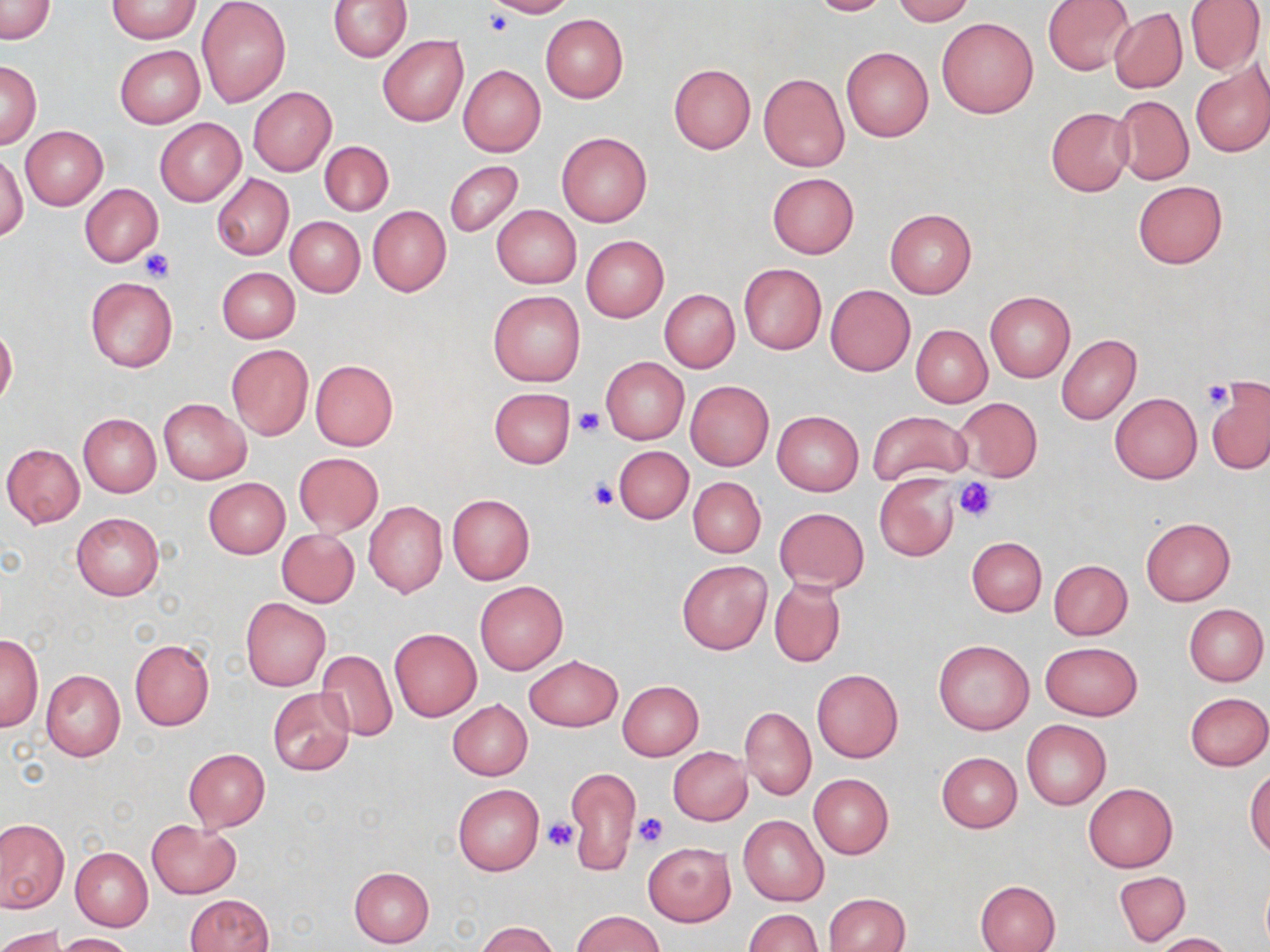

slide-level diagnosis = negative for blood parasites
uninfected red blood cell locations = approximate bounding boxes as named x1/y1/x2/y2 corners in pixels: (x1=108, y1=0, x2=200, y2=43), (x1=196, y1=0, x2=290, y2=107), (x1=483, y1=0, x2=576, y2=18), (x1=804, y1=0, x2=894, y2=16), (x1=890, y1=0, x2=974, y2=24), (x1=1043, y1=0, x2=1135, y2=74), (x1=1185, y1=0, x2=1265, y2=76), (x1=0, y1=1, x2=55, y2=43), (x1=329, y1=1, x2=412, y2=61), (x1=1109, y1=8, x2=1187, y2=93), (x1=540, y1=14, x2=628, y2=103), (x1=937, y1=17, x2=1039, y2=118), (x1=377, y1=36, x2=469, y2=126), (x1=115, y1=45, x2=205, y2=128), (x1=841, y1=47, x2=933, y2=141), (x1=1, y1=61, x2=41, y2=148), (x1=668, y1=63, x2=756, y2=153), (x1=1191, y1=64, x2=1270, y2=157), (x1=458, y1=65, x2=546, y2=158), (x1=759, y1=73, x2=849, y2=171), (x1=248, y1=86, x2=335, y2=176), (x1=1113, y1=95, x2=1194, y2=186), (x1=1045, y1=107, x2=1134, y2=196), (x1=155, y1=118, x2=245, y2=206), (x1=21, y1=126, x2=108, y2=210), (x1=557, y1=132, x2=652, y2=227), (x1=319, y1=141, x2=392, y2=216), (x1=0, y1=151, x2=26, y2=242), (x1=444, y1=160, x2=523, y2=237), (x1=210, y1=173, x2=294, y2=261), (x1=766, y1=173, x2=858, y2=259), (x1=1132, y1=180, x2=1227, y2=269), (x1=80, y1=183, x2=162, y2=267), (x1=491, y1=205, x2=581, y2=289), (x1=368, y1=206, x2=451, y2=296), (x1=885, y1=209, x2=977, y2=298), (x1=285, y1=216, x2=365, y2=297), (x1=581, y1=236, x2=669, y2=323), (x1=739, y1=263, x2=826, y2=354), (x1=217, y1=267, x2=299, y2=343), (x1=84, y1=276, x2=178, y2=373), (x1=825, y1=284, x2=916, y2=376), (x1=488, y1=290, x2=585, y2=386), (x1=660, y1=290, x2=739, y2=372), (x1=985, y1=291, x2=1075, y2=382), (x1=0, y1=324, x2=17, y2=407), (x1=911, y1=325, x2=992, y2=407), (x1=1057, y1=335, x2=1142, y2=425), (x1=226, y1=343, x2=313, y2=440), (x1=601, y1=357, x2=688, y2=444), (x1=309, y1=359, x2=398, y2=451), (x1=1207, y1=379, x2=1270, y2=474), (x1=686, y1=381, x2=774, y2=470), (x1=489, y1=387, x2=577, y2=469), (x1=1109, y1=393, x2=1201, y2=484), (x1=954, y1=397, x2=1043, y2=480), (x1=158, y1=399, x2=250, y2=484), (x1=772, y1=410, x2=863, y2=495), (x1=867, y1=410, x2=972, y2=485), (x1=78, y1=413, x2=161, y2=497), (x1=2, y1=444, x2=85, y2=528), (x1=612, y1=445, x2=693, y2=523), (x1=293, y1=452, x2=383, y2=536), (x1=874, y1=474, x2=959, y2=561), (x1=688, y1=477, x2=765, y2=557), (x1=203, y1=478, x2=290, y2=558), (x1=447, y1=495, x2=535, y2=584), (x1=363, y1=500, x2=447, y2=598), (x1=774, y1=507, x2=870, y2=593), (x1=71, y1=513, x2=164, y2=602), (x1=1140, y1=517, x2=1235, y2=606), (x1=276, y1=529, x2=359, y2=607), (x1=966, y1=536, x2=1047, y2=616), (x1=677, y1=560, x2=772, y2=654), (x1=1048, y1=560, x2=1132, y2=640), (x1=769, y1=577, x2=846, y2=668), (x1=475, y1=582, x2=567, y2=674), (x1=241, y1=598, x2=330, y2=691), (x1=1185, y1=605, x2=1267, y2=686), (x1=389, y1=629, x2=481, y2=721), (x1=1, y1=634, x2=43, y2=730), (x1=130, y1=639, x2=215, y2=730), (x1=933, y1=639, x2=1034, y2=735), (x1=1041, y1=642, x2=1143, y2=721), (x1=316, y1=650, x2=398, y2=741), (x1=524, y1=655, x2=623, y2=732), (x1=812, y1=669, x2=903, y2=763), (x1=41, y1=670, x2=124, y2=763), (x1=617, y1=680, x2=703, y2=760), (x1=267, y1=688, x2=355, y2=775), (x1=1184, y1=692, x2=1270, y2=770), (x1=447, y1=699, x2=532, y2=780), (x1=741, y1=707, x2=816, y2=801), (x1=1021, y1=719, x2=1111, y2=810), (x1=668, y1=747, x2=751, y2=826), (x1=183, y1=748, x2=269, y2=832), (x1=937, y1=752, x2=1022, y2=832), (x1=565, y1=768, x2=642, y2=876), (x1=1246, y1=769, x2=1270, y2=857), (x1=808, y1=773, x2=893, y2=859), (x1=453, y1=783, x2=544, y2=876), (x1=1083, y1=783, x2=1177, y2=872), (x1=738, y1=815, x2=828, y2=907), (x1=0, y1=818, x2=69, y2=912), (x1=147, y1=819, x2=240, y2=898), (x1=643, y1=843, x2=735, y2=926), (x1=70, y1=846, x2=153, y2=931), (x1=349, y1=866, x2=434, y2=948), (x1=1114, y1=871, x2=1190, y2=946), (x1=976, y1=880, x2=1060, y2=951), (x1=824, y1=893, x2=910, y2=952), (x1=185, y1=894, x2=274, y2=952), (x1=745, y1=909, x2=824, y2=952), (x1=571, y1=910, x2=664, y2=952), (x1=475, y1=921, x2=561, y2=952), (x1=0, y1=926, x2=66, y2=952), (x1=58, y1=932, x2=139, y2=952), (x1=1153, y1=932, x2=1236, y2=952)
modality = optical microscopy
field of view = single
platelet locations = approximate bounding boxes as named x1/y1/x2/y2 corners in pixels: (x1=485, y1=11, x2=515, y2=37), (x1=137, y1=248, x2=175, y2=283), (x1=1202, y1=380, x2=1234, y2=409), (x1=572, y1=408, x2=605, y2=438), (x1=587, y1=478, x2=621, y2=510), (x1=955, y1=479, x2=998, y2=522), (x1=630, y1=811, x2=671, y2=849), (x1=543, y1=819, x2=576, y2=853)
magnification = 1000x
stain = May-Grünwald-Giemsa
image size = 1270×952 pixels
preparation = thin blood smear